Locate every parasitized red blood cell.
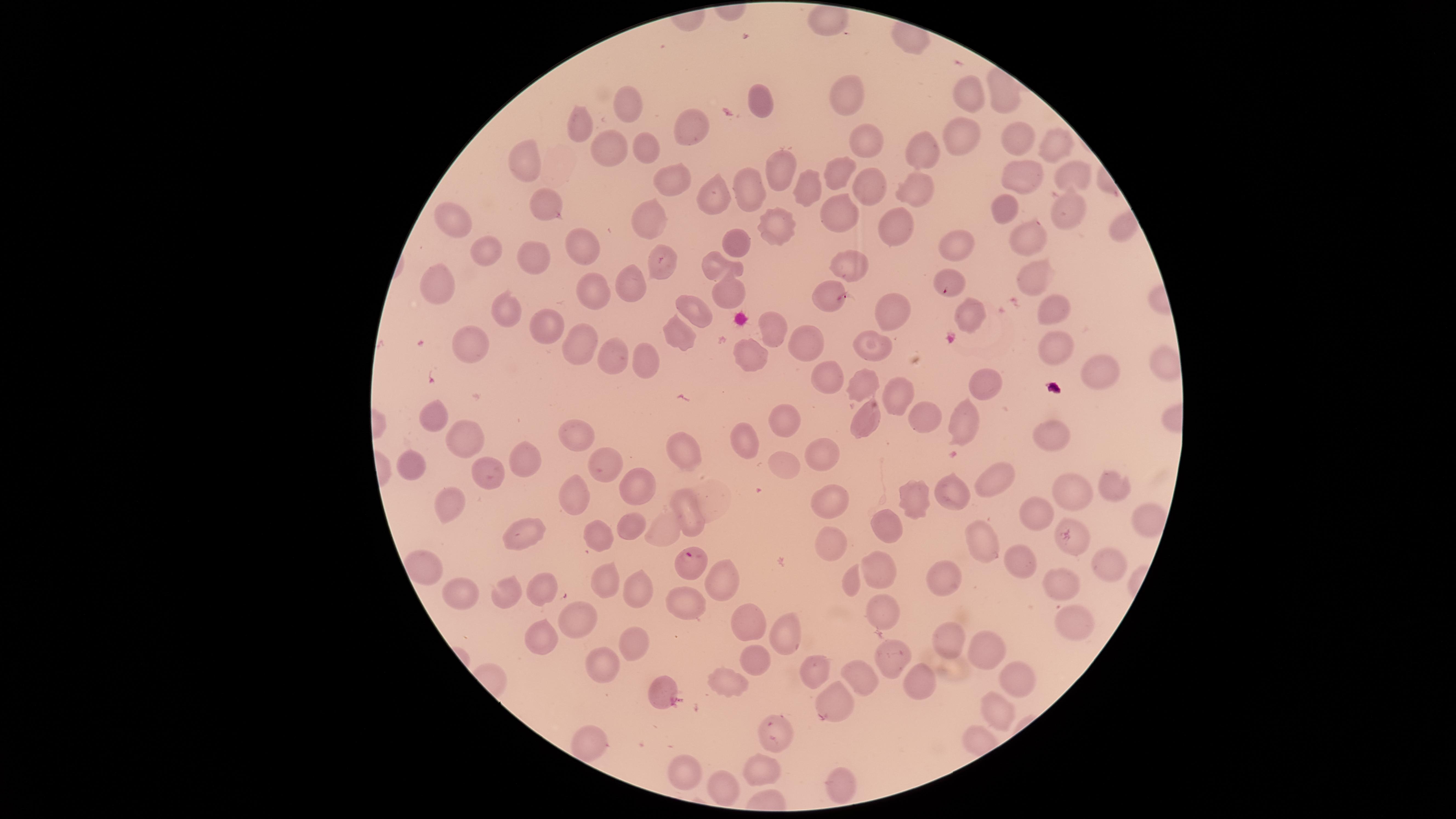

Approximate marker points, in pixels from the top-left corner.
Parasitized red blood cells: (x=690, y=563).

Approximate marker points, in pixels from the top-left corner.
Summary:
  - Uninfected red blood cells: (x=827, y=21), (x=972, y=94), (x=846, y=97), (x=759, y=101), (x=626, y=107), (x=578, y=130), (x=698, y=130), (x=961, y=135), (x=1013, y=139), (x=865, y=143), (x=652, y=146), (x=1053, y=149), (x=925, y=150), (x=596, y=153), (x=525, y=158), (x=840, y=176), (x=1069, y=176), (x=667, y=177), (x=776, y=179), (x=1019, y=179), (x=813, y=186), (x=869, y=189), (x=911, y=190), (x=713, y=193), (x=544, y=198), (x=749, y=198), (x=997, y=204), (x=1067, y=204), (x=648, y=219), (x=842, y=220), (x=452, y=225), (x=775, y=228), (x=890, y=229), (x=1032, y=239), (x=581, y=246), (x=728, y=248), (x=956, y=249), (x=494, y=255), (x=539, y=255), (x=663, y=261), (x=852, y=264), (x=713, y=266), (x=1040, y=275), (x=949, y=288), (x=591, y=290), (x=632, y=291), (x=824, y=291), (x=725, y=293), (x=441, y=295), (x=1050, y=306), (x=697, y=308), (x=890, y=308), (x=506, y=311), (x=967, y=314), (x=547, y=327), (x=769, y=331), (x=677, y=339), (x=806, y=341), (x=579, y=344), (x=876, y=349), (x=1057, y=350), (x=467, y=354), (x=607, y=358), (x=744, y=358), (x=644, y=361), (x=1171, y=362), (x=1101, y=370), (x=987, y=379), (x=829, y=380), (x=862, y=384), (x=896, y=396), (x=435, y=416), (x=787, y=419), (x=918, y=420), (x=866, y=421), (x=972, y=425), (x=464, y=430), (x=577, y=435), (x=1056, y=438), (x=741, y=442), (x=680, y=447), (x=817, y=454), (x=523, y=461), (x=409, y=464), (x=602, y=464), (x=787, y=469), (x=492, y=470), (x=995, y=475), (x=956, y=483), (x=1109, y=484), (x=638, y=486), (x=1076, y=493), (x=832, y=499), (x=572, y=500), (x=913, y=500), (x=449, y=503), (x=1029, y=509), (x=683, y=514), (x=1145, y=518), (x=891, y=524), (x=629, y=529), (x=523, y=533), (x=602, y=536), (x=984, y=536), (x=1075, y=542), (x=834, y=543), (x=1018, y=558), (x=1105, y=560), (x=422, y=566), (x=945, y=571), (x=877, y=573), (x=605, y=578), (x=718, y=578), (x=854, y=581), (x=1063, y=584), (x=635, y=585), (x=458, y=586), (x=543, y=588), (x=507, y=589), (x=684, y=604), (x=878, y=612), (x=578, y=618), (x=753, y=624), (x=1070, y=628), (x=787, y=634), (x=540, y=638), (x=949, y=639), (x=630, y=644), (x=889, y=658), (x=984, y=658), (x=602, y=664), (x=753, y=666), (x=811, y=673), (x=858, y=680), (x=723, y=681), (x=919, y=681), (x=660, y=686), (x=1021, y=686), (x=832, y=699), (x=996, y=716), (x=775, y=734), (x=584, y=743), (x=683, y=764), (x=763, y=770), (x=834, y=777), (x=728, y=787)
  - Field of view: single
  - Image size: 1456×819 pixels
  - Visible region: circular
  - Capture: smartphone photograph through the microscope eyepiece
  - Stain: Giemsa
  - Species: Plasmodium falciparum
  - Preparation: thin blood smear